Report the malaria status of this cell.
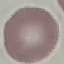

It is uninfected.

capture = smartphone through the microscope eyepiece
image type = cell patch, automatically extracted from a larger field of view and resized to 64 × 64 pixels
stain = Giemsa
preparation = thin blood smear